Comment on the morphology of the erythrocytes.
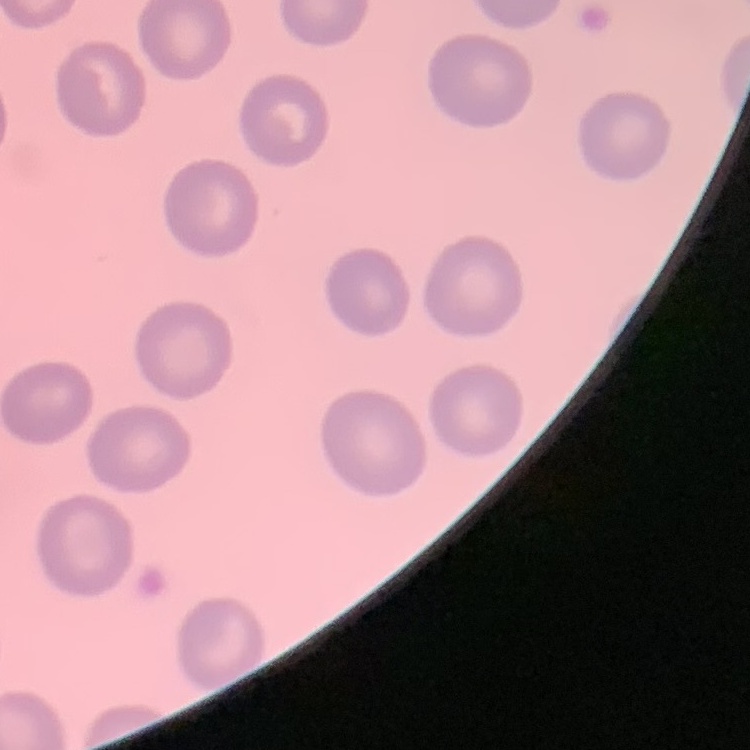

No rouleaux formation.

Summary:
  - Image type: one tile cut from a larger photomicrograph
  - Preparation: thin peripheral smear
  - Stain: Field's or Giemsa